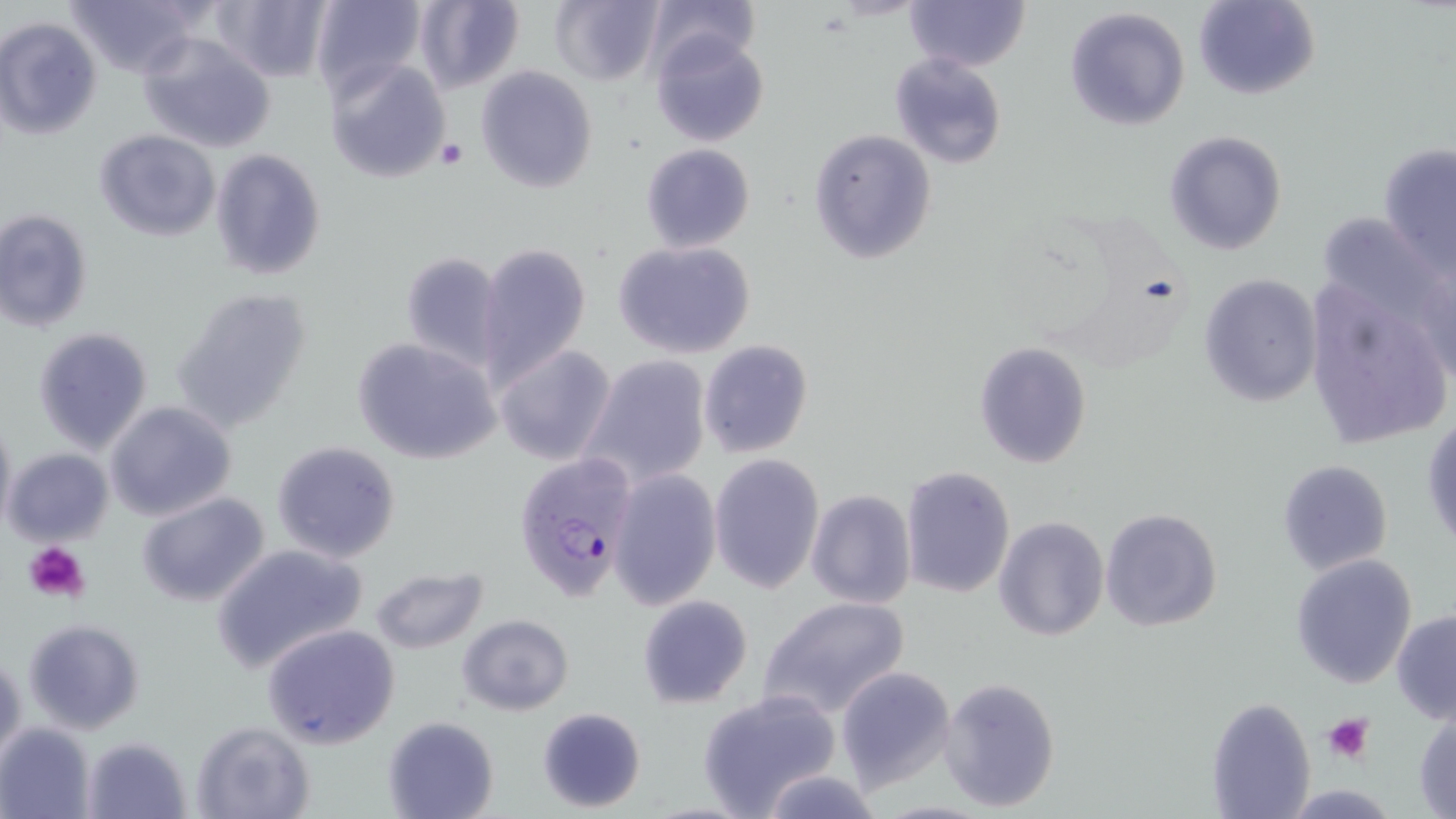
{
  "plasmodium_falciparum_infected_red_blood_cell_locations": "approximate bounding boxes as [x1, y1, x2, y2] in pixels: [514, 454, 639, 603]",
  "slide_level_diagnosis": "Plasmodium falciparum",
  "preparation": "thin blood smear",
  "image_size": "1456×819 pixels",
  "magnification": "1000x",
  "modality": "light microscopy",
  "uninfected_red_blood_cell_locations": "approximate bounding boxes as [x1, y1, x2, y2] in pixels: [62, 0, 205, 78], [211, 0, 331, 82], [310, 0, 428, 101], [413, 0, 525, 96], [550, 0, 664, 87], [643, 0, 759, 78], [905, 0, 1030, 71], [1195, 0, 1318, 99], [1064, 6, 1189, 131], [0, 17, 102, 139], [649, 32, 769, 147], [138, 34, 276, 153], [889, 52, 1007, 170], [324, 57, 452, 186], [476, 65, 597, 192], [95, 128, 220, 240], [807, 129, 937, 263], [1164, 130, 1287, 255], [1378, 141, 1456, 278], [641, 143, 755, 253], [210, 147, 327, 280], [0, 209, 93, 332], [611, 240, 757, 359], [475, 243, 591, 385], [398, 251, 506, 371], [1198, 272, 1323, 408], [1303, 273, 1453, 451], [171, 286, 314, 433], [32, 327, 154, 453], [352, 337, 502, 466], [698, 339, 813, 459], [974, 342, 1091, 468], [492, 343, 616, 466], [580, 355, 711, 487], [105, 400, 237, 521], [0, 411, 16, 537], [1423, 412, 1455, 553], [271, 440, 402, 565], [3, 448, 114, 546], [709, 454, 824, 595], [1277, 459, 1394, 575], [899, 467, 1015, 598], [608, 468, 722, 612], [805, 490, 917, 609], [137, 492, 271, 607], [787, 495, 916, 710], [1099, 506, 1222, 633], [992, 516, 1109, 643], [211, 543, 369, 673], [1291, 553, 1418, 687], [370, 565, 488, 654], [637, 594, 753, 709], [756, 594, 912, 723], [1391, 609, 1456, 724], [457, 614, 575, 715], [22, 618, 145, 734], [263, 623, 401, 750], [1, 651, 24, 764], [837, 666, 956, 791], [939, 677, 1060, 812], [696, 689, 841, 817], [1206, 696, 1316, 818], [536, 706, 646, 813], [1412, 708, 1456, 817], [382, 715, 499, 819], [189, 720, 315, 819], [0, 722, 96, 819], [83, 736, 191, 817], [759, 770, 882, 818]",
  "platelet_locations": "approximate bounding boxes as [x1, y1, x2, y2] in pixels: [434, 137, 468, 170], [24, 541, 92, 603], [1324, 713, 1373, 764]",
  "stain": "May-Grünwald-Giemsa",
  "field_of_view": "one of a larger specimen"
}